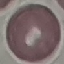
Summary:
  - Result: no malaria parasites seen
  - Stain: Giemsa
  - Capture: smartphone through the microscope eyepiece
  - Image type: cell patch, automatically extracted from a larger field of view and resized to 64 × 64 pixels
  - Preparation: thin blood smear